Assess the morphology of the red blood cells.
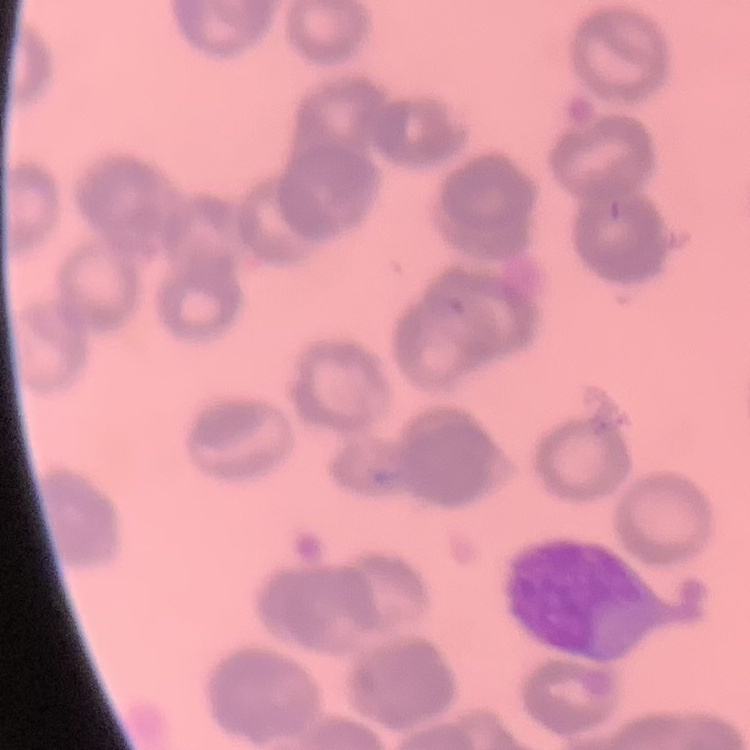

Rouleaux formation.

Summary:
  - Image type: square crop of a larger photomicrograph
  - Preparation: thin peripheral smear
  - Stain: Field's or Giemsa